Assess the morphology of the red blood cells.
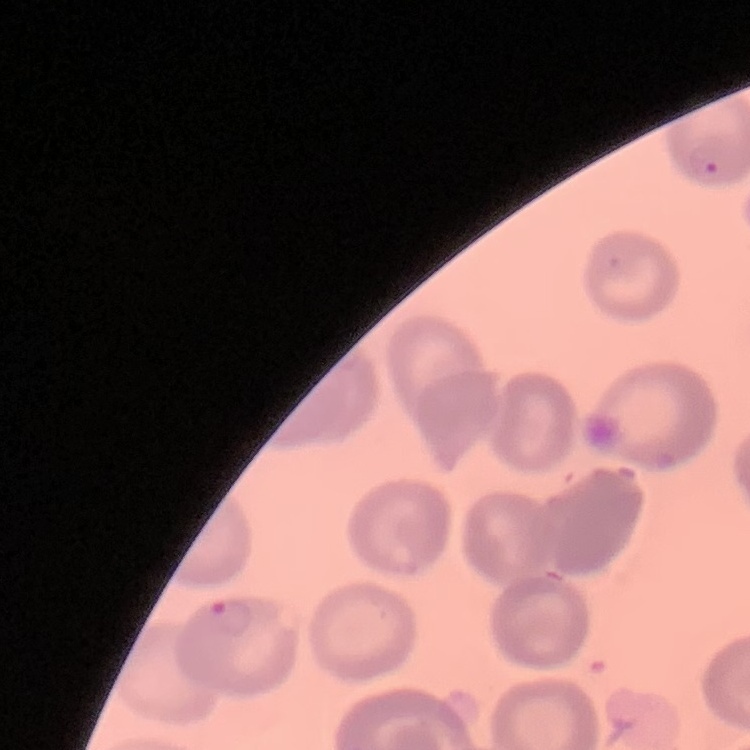

They show no rouleaux formation.

Summary:
  - Stain: Field's or Giemsa
  - Preparation: thin blood smear
  - Image type: square crop of a larger photomicrograph